State which parasite is depicted.
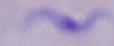

A trypanosome.

modality = photomicrograph
magnification = 1000x